Assess the morphology of the erythrocytes.
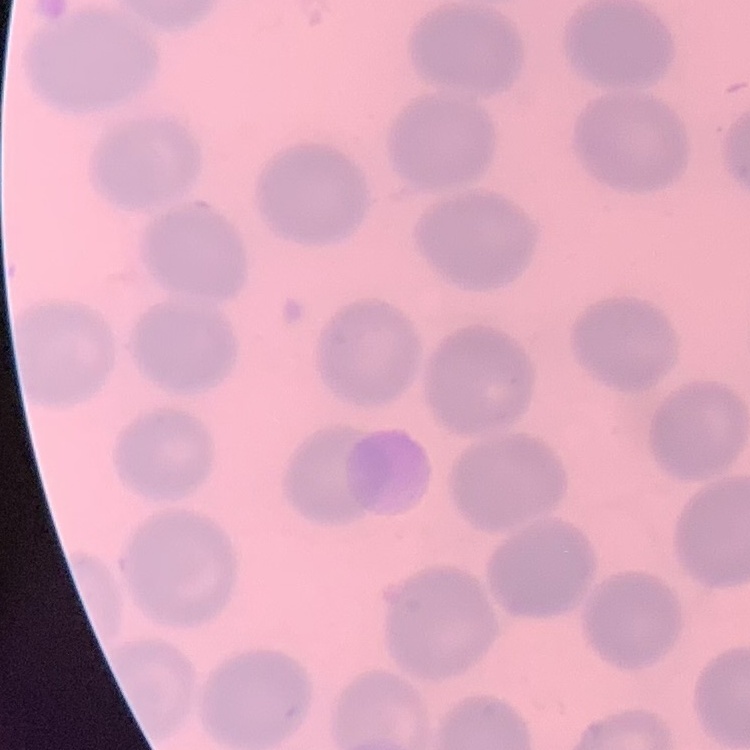

They show no rouleaux formation.

Stained with either Field's or Giemsa. Thin peripheral smear. One tile cut from a larger photomicrograph.